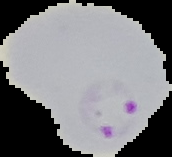

malaria_status: parasitized
preparation: thin blood smear
image_type: segmented cell region with the area outside set to black
image_size: 172×157 pixels